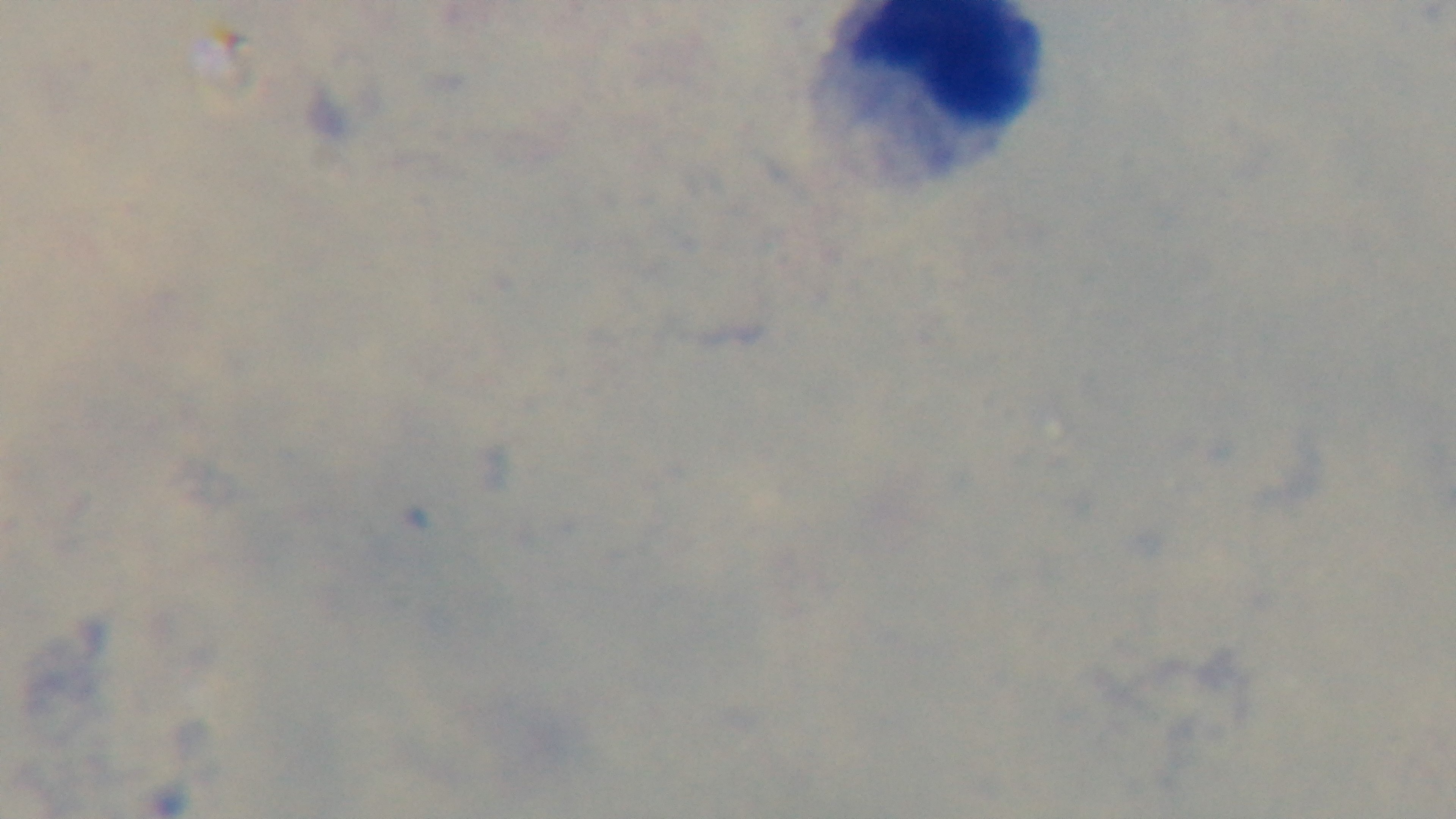

Summary:
  - Preparation: thick smear
  - Modality: light microscopy
  - Field of view: single
  - Capture: mounted 4K digital camera
  - Objective: 100x oil immersion
  - Stain: Giemsa
  - Malaria status: uninfected